Locate platelets.
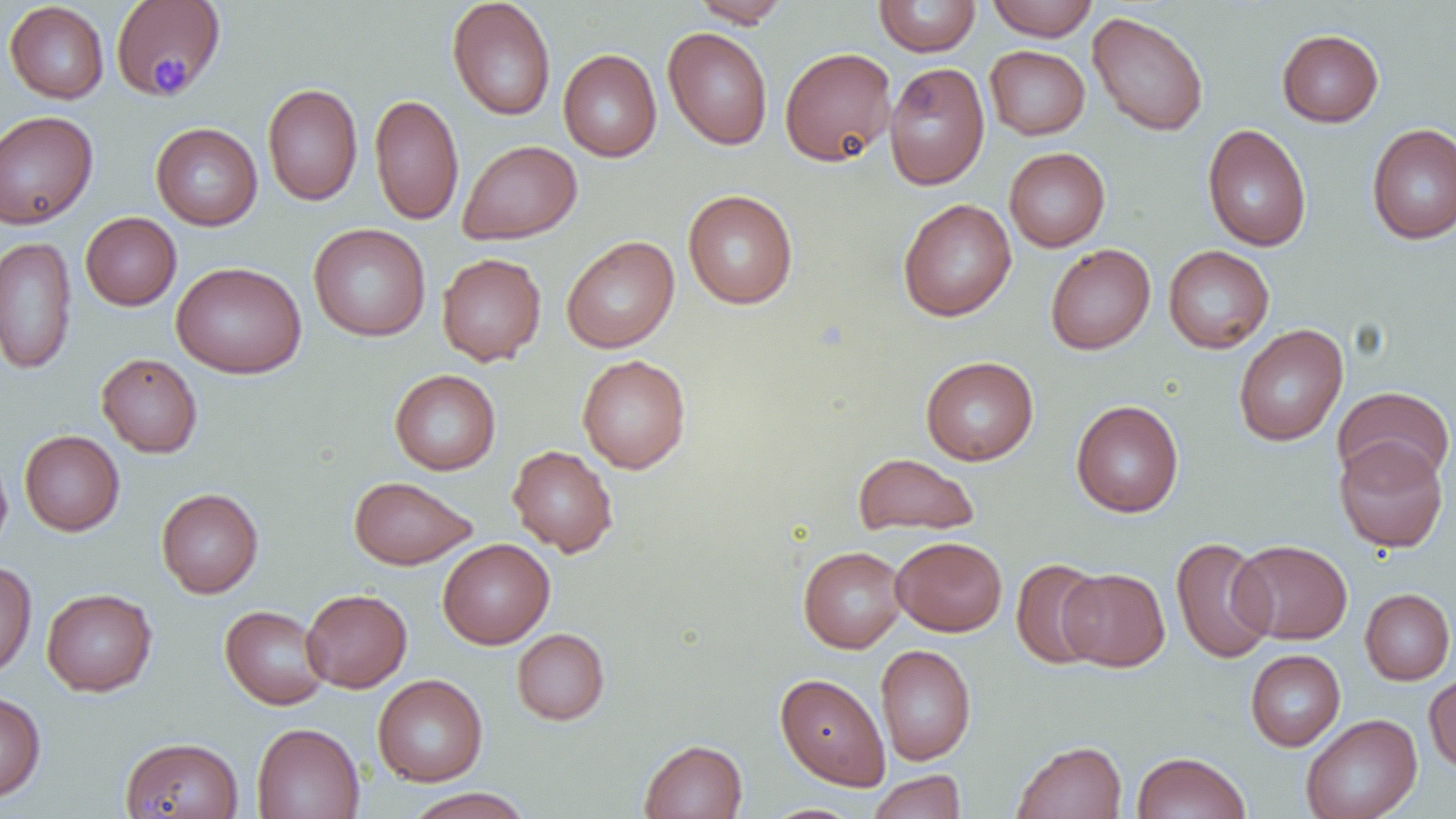

Approximate bounding boxes as (x1, y1, x2, y2) in pixels.
Platelets: (150, 53, 193, 95).

Uninfected red blood cell locations: (110, 0, 226, 98), (691, 0, 791, 27), (873, 0, 981, 56), (986, 0, 1098, 41), (4, 1, 109, 104), (447, 1, 556, 121), (1088, 11, 1209, 136), (663, 27, 773, 150), (1277, 29, 1384, 127), (985, 45, 1090, 140), (779, 46, 896, 166), (558, 48, 662, 162), (799, 56, 975, 178), (884, 62, 990, 190), (262, 83, 363, 206), (369, 93, 464, 226), (0, 111, 99, 229), (151, 122, 263, 230), (1366, 123, 1456, 244), (1202, 124, 1312, 252), (458, 139, 582, 244), (1004, 147, 1110, 252), (683, 189, 798, 309), (898, 198, 1017, 321), (80, 212, 181, 310), (308, 223, 431, 342), (0, 236, 77, 375), (561, 236, 679, 353), (1045, 243, 1155, 354), (1163, 245, 1274, 354), (437, 253, 546, 366), (171, 262, 307, 379), (1233, 324, 1348, 446), (96, 353, 203, 458), (577, 354, 691, 474), (920, 356, 1039, 465), (389, 369, 501, 475), (1333, 386, 1455, 488), (1071, 399, 1184, 517), (19, 430, 125, 535), (1334, 437, 1449, 553), (507, 444, 618, 557), (0, 450, 13, 557), (852, 453, 979, 536), (348, 476, 477, 570), (156, 487, 264, 598), (891, 536, 1007, 636), (1170, 537, 1276, 664), (438, 538, 554, 649), (1230, 539, 1353, 644), (798, 546, 907, 653), (1010, 559, 1107, 669), (0, 561, 37, 679), (1059, 568, 1169, 671), (42, 588, 157, 696), (301, 588, 412, 692), (1360, 588, 1455, 685), (220, 605, 330, 710), (512, 628, 610, 725), (875, 644, 976, 766), (1245, 649, 1345, 751), (1424, 671, 1456, 773), (775, 673, 891, 790), (372, 674, 488, 786), (0, 691, 46, 803), (1300, 714, 1422, 819), (251, 722, 365, 819), (120, 736, 243, 818), (639, 739, 747, 819), (1013, 740, 1127, 819), (1131, 751, 1251, 819), (867, 770, 967, 819), (402, 787, 534, 819), (761, 804, 866, 819). Slide-level diagnosis: no evidence of blood parasites. Light microscopy. Captured at 1000x magnification. Thin blood film. Image is 1456×819 pixels. Single field of view.